Assess the morphology of the red blood cells.
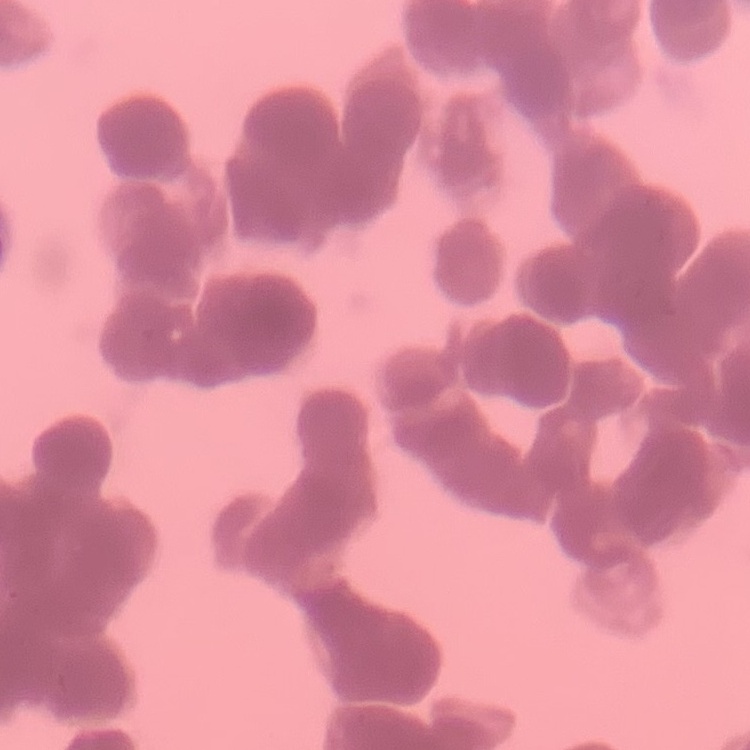

They show rouleaux formation.

Field's or Giemsa stain. One tile cut from a larger photomicrograph. Thin peripheral smear.